Report the malaria status of this cell.
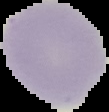

Uninfected.

Summary:
  - Preparation: thin blood film
  - Image type: segmented cell region on a black background
  - Image size: 109×112 pixels